State the blood parasite species.
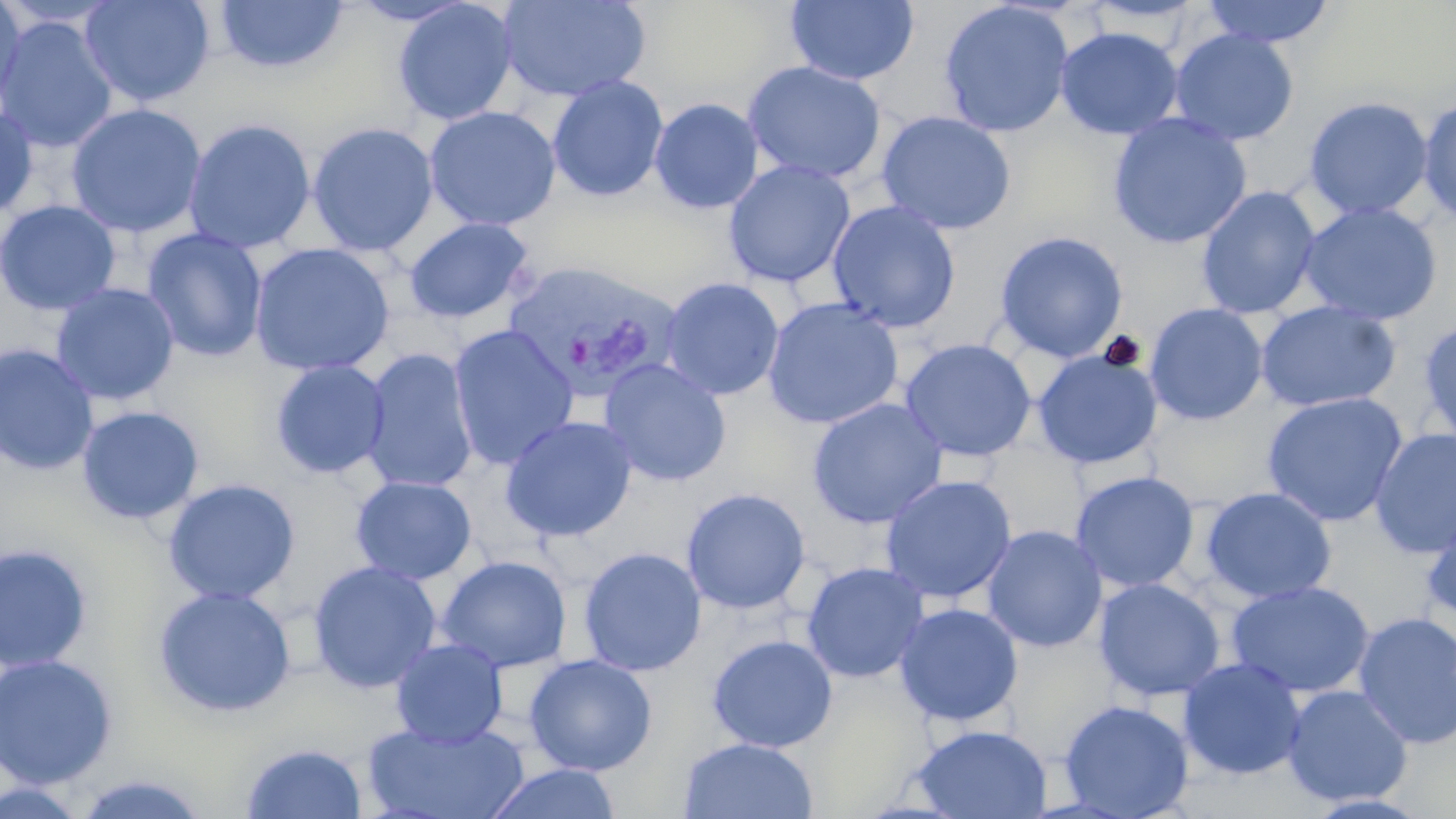
Plasmodium vivax.

Approximate bounding boxes as (x1,y1)-(x2,y2) corner pairs in pixels. Uninfected red blood cell locations: (0,0)-(26,117), (78,0)-(216,107), (346,0)-(476,26), (498,0)-(651,103), (785,0)-(919,86), (1200,0)-(1336,49), (0,1)-(123,29), (214,1)-(348,73), (392,1)-(519,126), (938,1)-(1074,137), (768,4)-(911,157), (0,16)-(118,154), (1055,26)-(1183,140), (1169,29)-(1299,146), (743,61)-(886,185), (546,76)-(669,202), (1417,96)-(1456,225), (1304,97)-(1433,220), (649,98)-(764,214), (66,103)-(206,238), (0,104)-(38,222), (424,106)-(561,231), (877,111)-(1017,235), (1108,113)-(1252,250), (183,118)-(316,254), (307,122)-(439,257), (723,160)-(855,288), (1196,187)-(1321,319), (0,200)-(121,315), (827,201)-(961,333), (1299,202)-(1442,325), (404,217)-(535,324), (141,228)-(268,363), (994,231)-(1128,362), (249,242)-(395,376), (660,277)-(784,401), (50,283)-(180,406), (763,297)-(904,429), (1255,302)-(1400,412), (1144,303)-(1269,426), (1417,319)-(1456,449), (448,324)-(578,470), (900,338)-(1037,462), (0,344)-(99,475), (360,348)-(478,494), (1032,349)-(1163,469), (269,359)-(390,479), (599,359)-(732,487), (1261,392)-(1409,527), (807,398)-(947,529), (77,405)-(205,524), (500,416)-(637,541), (1369,428)-(1456,558), (1070,471)-(1199,592), (880,475)-(1017,604), (350,476)-(478,585), (163,478)-(301,605), (682,487)-(811,615), (1200,487)-(1337,604), (1422,508)-(1456,626), (982,525)-(1107,653), (0,543)-(94,671), (578,547)-(706,676), (436,555)-(572,674), (307,560)-(442,694), (802,562)-(930,683), (1093,578)-(1226,701), (1226,581)-(1375,698), (152,585)-(296,717), (894,603)-(1023,726), (1352,611)-(1456,749), (707,634)-(838,753), (390,638)-(508,747), (524,654)-(657,776), (0,655)-(118,789), (1178,658)-(1306,780), (1282,685)-(1414,807), (1058,699)-(1195,818), (363,720)-(529,818), (910,724)-(1052,818), (678,737)-(818,819), (240,742)-(368,818), (484,763)-(622,819), (70,772)-(211,818), (0,776)-(90,817), (1302,793)-(1433,818). Plasmodium vivax-infected red blood cell locations: (500,259)-(680,401). 1000x magnification. May-Grünwald-Giemsa stain. Optical microscopy. Thin blood smear. Image is 1456×819 pixels. One field of a larger specimen.